Outline each uninfected red blood cell.
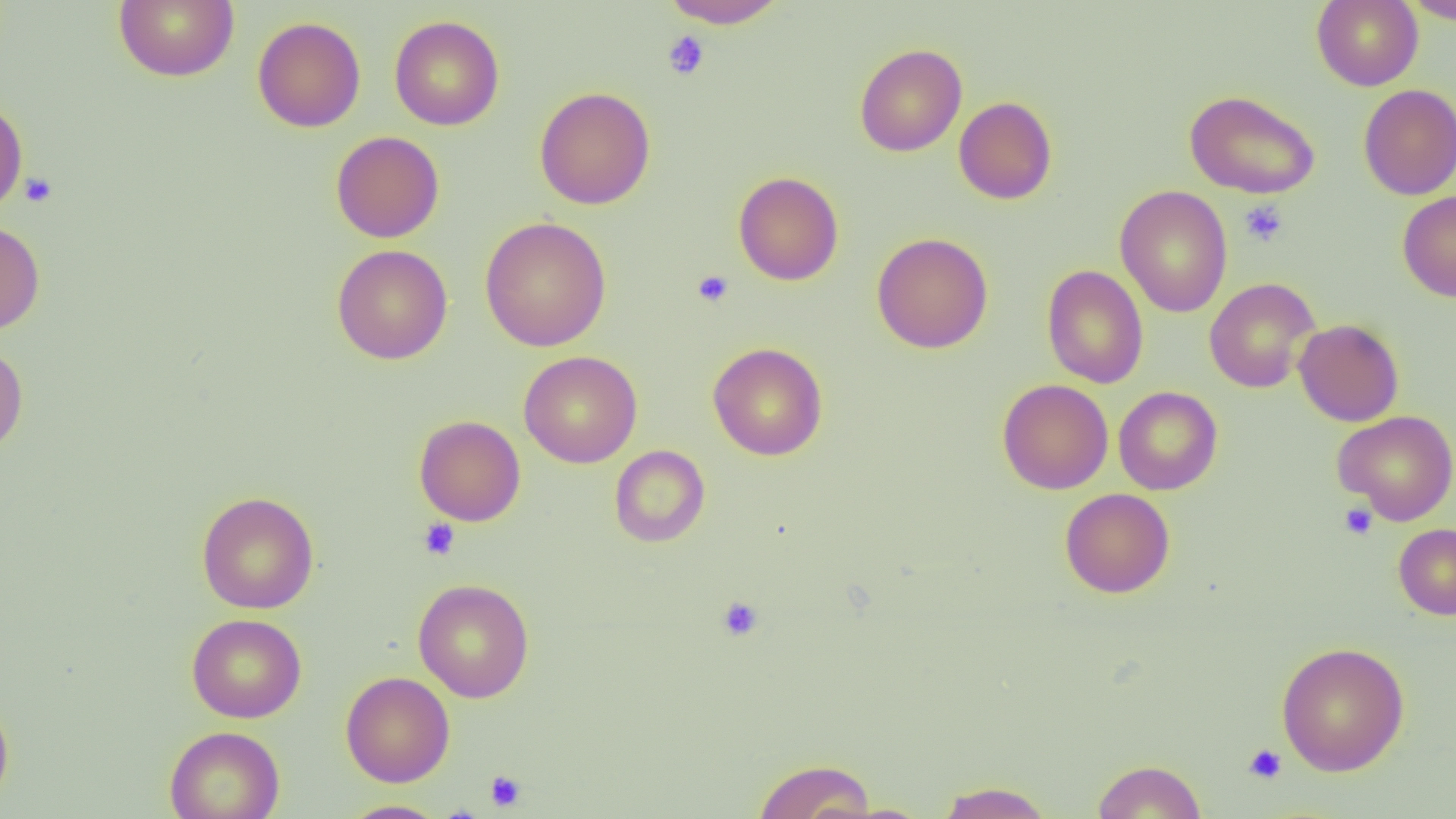
Approximate bounding boxes as [x1, y1, x2, y2] in pixels.
Uninfected red blood cells: [113, 0, 239, 82], [659, 0, 790, 29], [1311, 0, 1423, 91], [1402, 0, 1456, 24], [389, 15, 505, 131], [252, 16, 366, 132], [854, 43, 967, 156], [1358, 84, 1456, 199], [534, 86, 656, 209], [1184, 90, 1321, 199], [954, 96, 1057, 204], [0, 98, 28, 215], [331, 131, 445, 243], [733, 171, 844, 285], [1115, 185, 1232, 318], [1397, 190, 1456, 301], [480, 216, 611, 351], [0, 219, 45, 335], [871, 232, 993, 353], [332, 244, 453, 364], [1041, 264, 1149, 389], [1204, 278, 1320, 394], [1293, 318, 1404, 426], [0, 341, 28, 456], [707, 342, 828, 460], [519, 350, 642, 468], [997, 378, 1114, 494], [1114, 386, 1223, 495], [1332, 410, 1456, 525], [414, 415, 526, 526], [609, 445, 710, 547], [1060, 488, 1175, 598], [196, 491, 320, 614], [1393, 523, 1456, 620], [413, 578, 534, 703], [186, 613, 307, 723], [1276, 641, 1410, 776], [340, 671, 455, 787], [0, 694, 14, 810], [165, 726, 285, 819], [753, 758, 876, 819], [1092, 759, 1207, 818], [936, 780, 1054, 819], [340, 800, 447, 818].

slide_level_diagnosis: no evidence of blood parasites
image_size: 1456×819 pixels
modality: light microscopy
field_of_view: one of a larger specimen
magnification: 1000x
preparation: thin blood film
platelet_locations: 'approximate bounding boxes as [x1, y1, x2, y2] in pixels: [662, 30, 710, 80], [20, 171, 58, 207], [1239, 199, 1289, 247], [692, 270, 734, 307], [1339, 503, 1378, 540], [418, 518, 461, 561], [716, 596, 764, 641], [1243, 744, 1287, 784], [485, 770, 526, 811]'